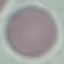 Malaria status: uninfected. Thin smear of blood. Acquired by smartphone through the microscope eyepiece. Giemsa-stained preparation. Cell patch, automatically extracted from a larger field of view and resized to 64 × 64 pixels.